Name the cell type shown.
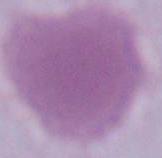

An erythrocyte.

Summary:
  - Magnification: 1000x
  - Modality: micrograph